Identify the parasite.
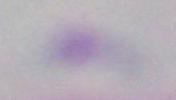
Toxoplasma gondii.

modality = micrograph
magnification = 1000x